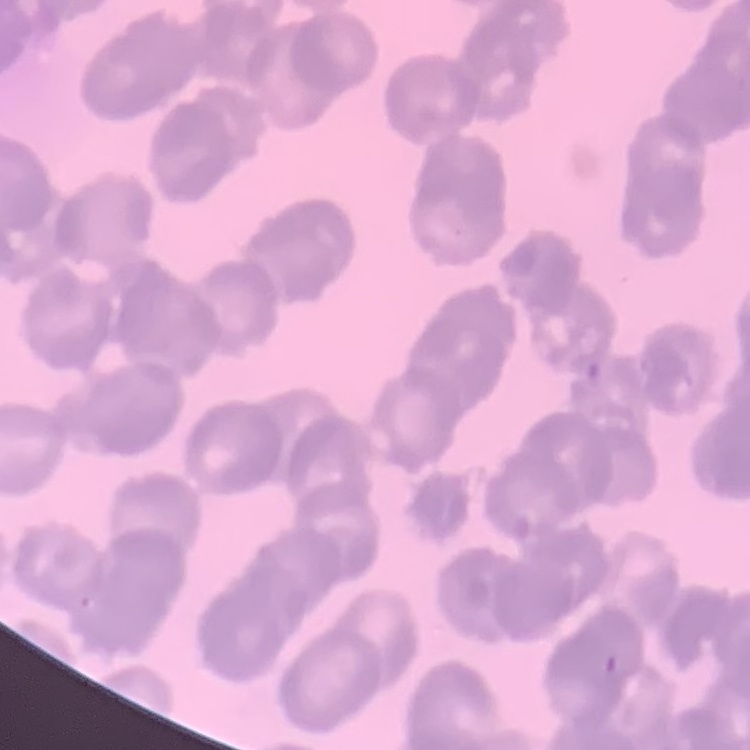

red_blood_cell_morphology: rouleaux formation
image_type: square crop of a larger photomicrograph
preparation: thin blood smear
stain: Field's or Giemsa